Name the parasite shown.
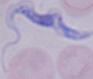
This is a trypanosome.

modality = micrograph
magnification = 1000x